Describe the morphology of the red blood cells.
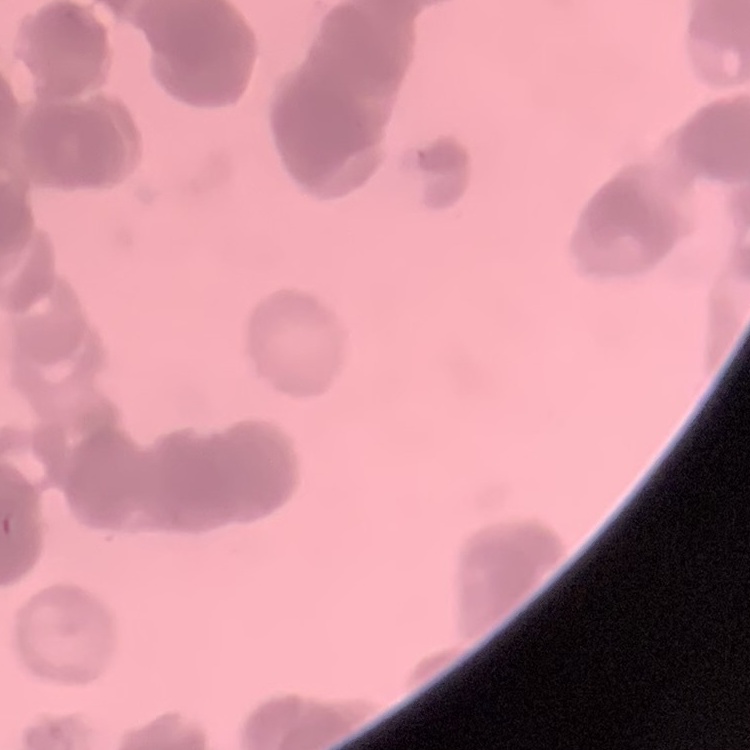
Rouleaux formation.

Stained with either Field's or Giemsa. Thin blood smear. One tile cut from a larger photomicrograph.